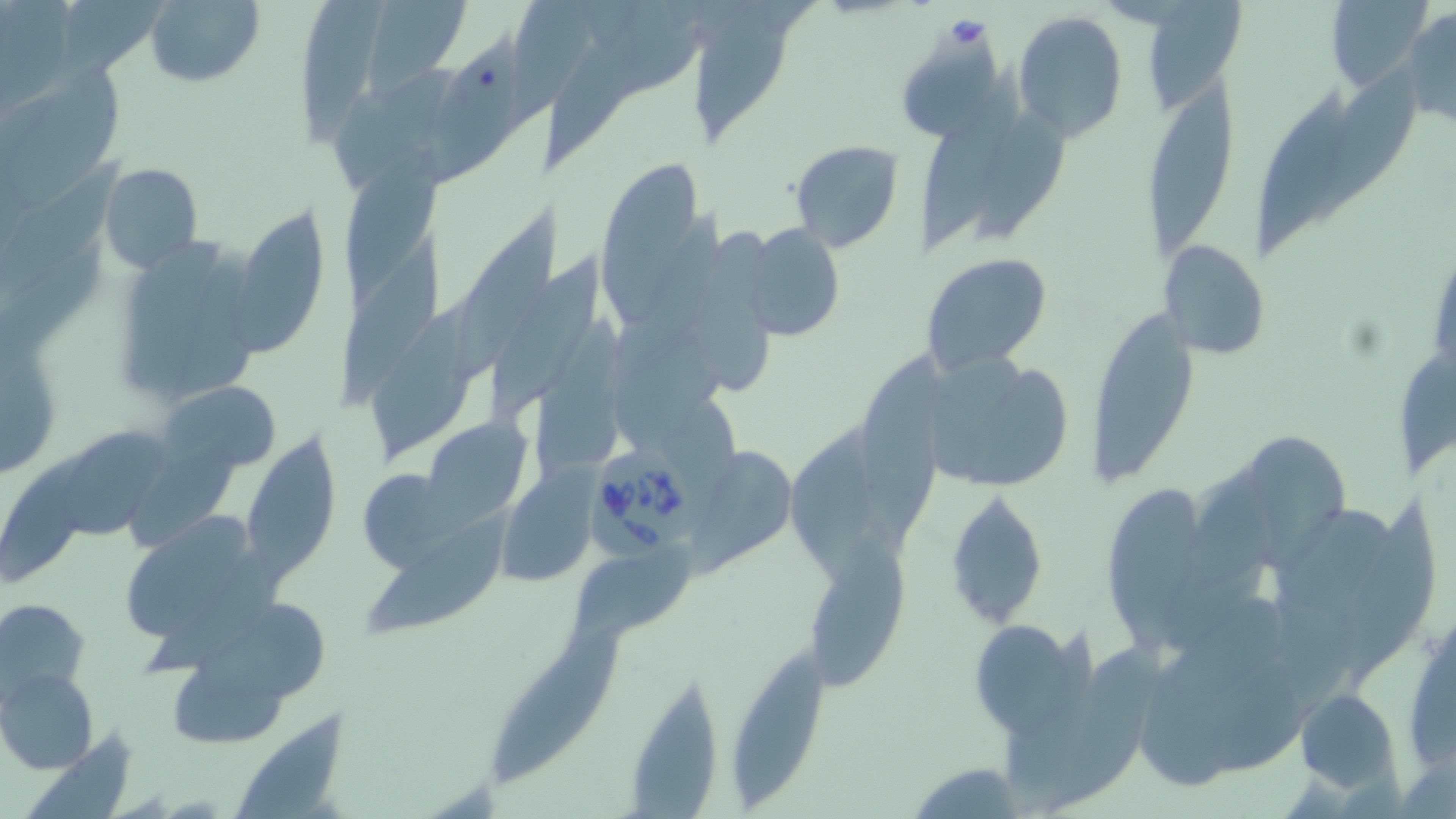
slide-level diagnosis = Babesia divergens
stain = May-Grünwald-Giemsa
magnification = 1000x
field of view = one of a larger specimen
uninfected red blood cell locations = approximate bounding boxes as (x1, y1, x2, y2) in pixels: (1132, 0, 1247, 113), (144, 1, 264, 88), (360, 1, 474, 102), (692, 1, 802, 144), (299, 2, 387, 151), (1323, 2, 1435, 91), (1401, 5, 1456, 128), (1012, 11, 1129, 142), (535, 27, 659, 173), (427, 34, 527, 183), (6, 60, 129, 210), (916, 68, 1029, 250), (1145, 74, 1239, 263), (1256, 91, 1351, 255), (968, 111, 1075, 237), (789, 138, 906, 253), (342, 146, 446, 304), (595, 158, 706, 303), (1, 161, 129, 307), (98, 161, 203, 273), (232, 201, 331, 353), (454, 204, 563, 387), (739, 222, 846, 339), (335, 234, 448, 409), (109, 236, 267, 413), (1157, 240, 1270, 359), (486, 247, 608, 417), (922, 251, 1054, 374), (360, 295, 487, 467), (1086, 302, 1202, 483), (1, 312, 64, 482), (1400, 346, 1456, 480), (918, 348, 1072, 493), (858, 349, 955, 560), (160, 380, 282, 475), (424, 416, 531, 516), (56, 430, 173, 540), (236, 431, 339, 581), (1252, 432, 1352, 569), (693, 445, 797, 573), (361, 470, 487, 580), (496, 473, 598, 587), (946, 488, 1047, 626), (1105, 488, 1206, 660), (1340, 499, 1437, 688), (116, 508, 272, 650), (367, 509, 512, 639), (810, 534, 913, 692), (572, 542, 697, 645), (1, 597, 91, 705), (192, 602, 331, 705), (1404, 613, 1456, 773), (967, 617, 1083, 736), (491, 618, 631, 782), (727, 645, 835, 796), (0, 668, 100, 774), (623, 672, 725, 814), (1296, 688, 1403, 795), (227, 708, 350, 819), (904, 761, 1030, 817)
preparation = thin blood smear
Babesia divergens-infected red blood cell locations = approximate bounding boxes as (x1, y1, x2, y2) in pixels: (585, 436, 694, 566)
image size = 1456×819 pixels
modality = light microscopy